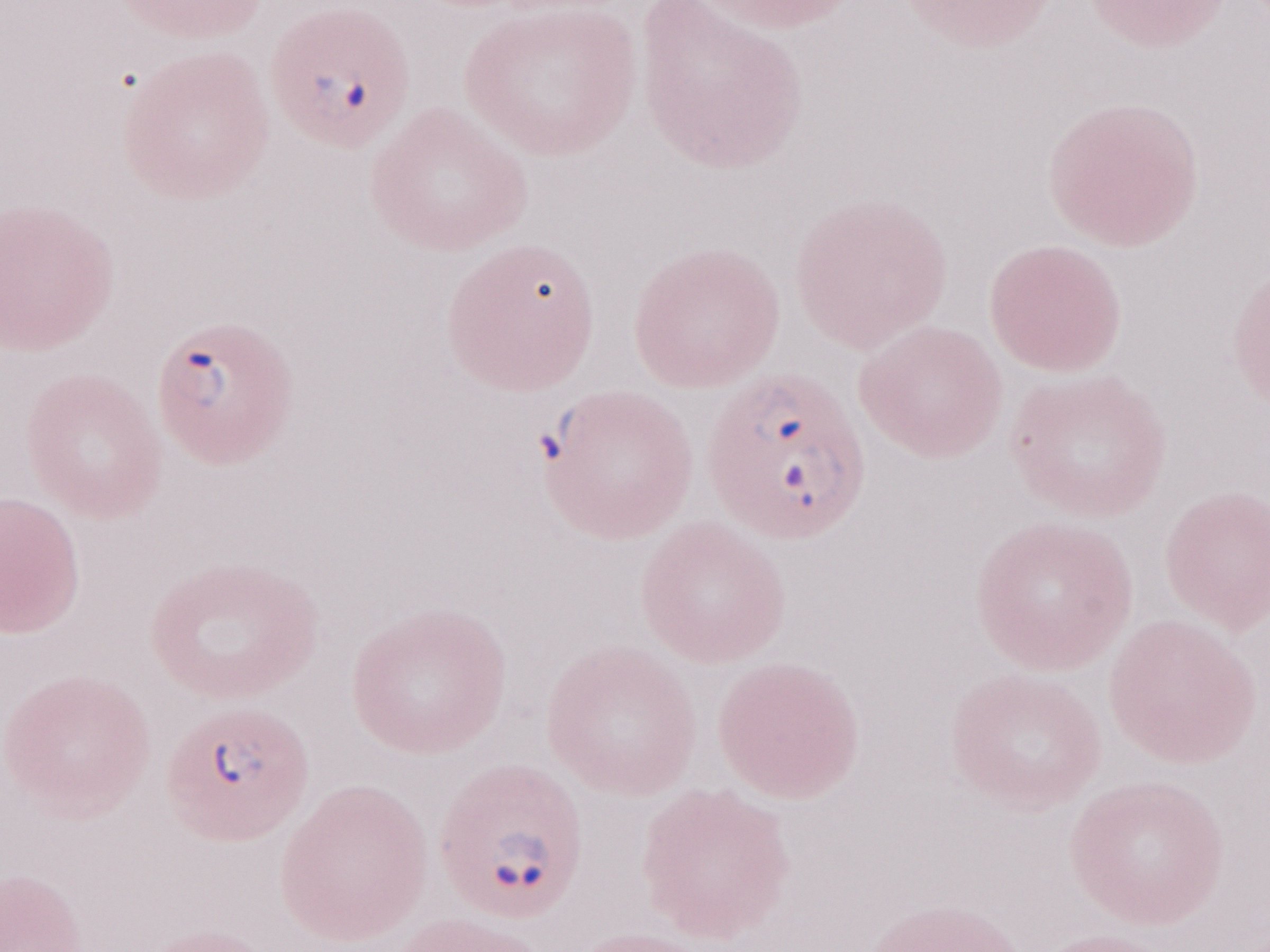 Olympus BX43 microscope and DP73 digital camera. Image is 1270×952 pixels. May-Grünwald-Giemsa stain. Patient-level malaria diagnosis: positive. One field of this slide. 1,000x magnification. Thin blood smear.